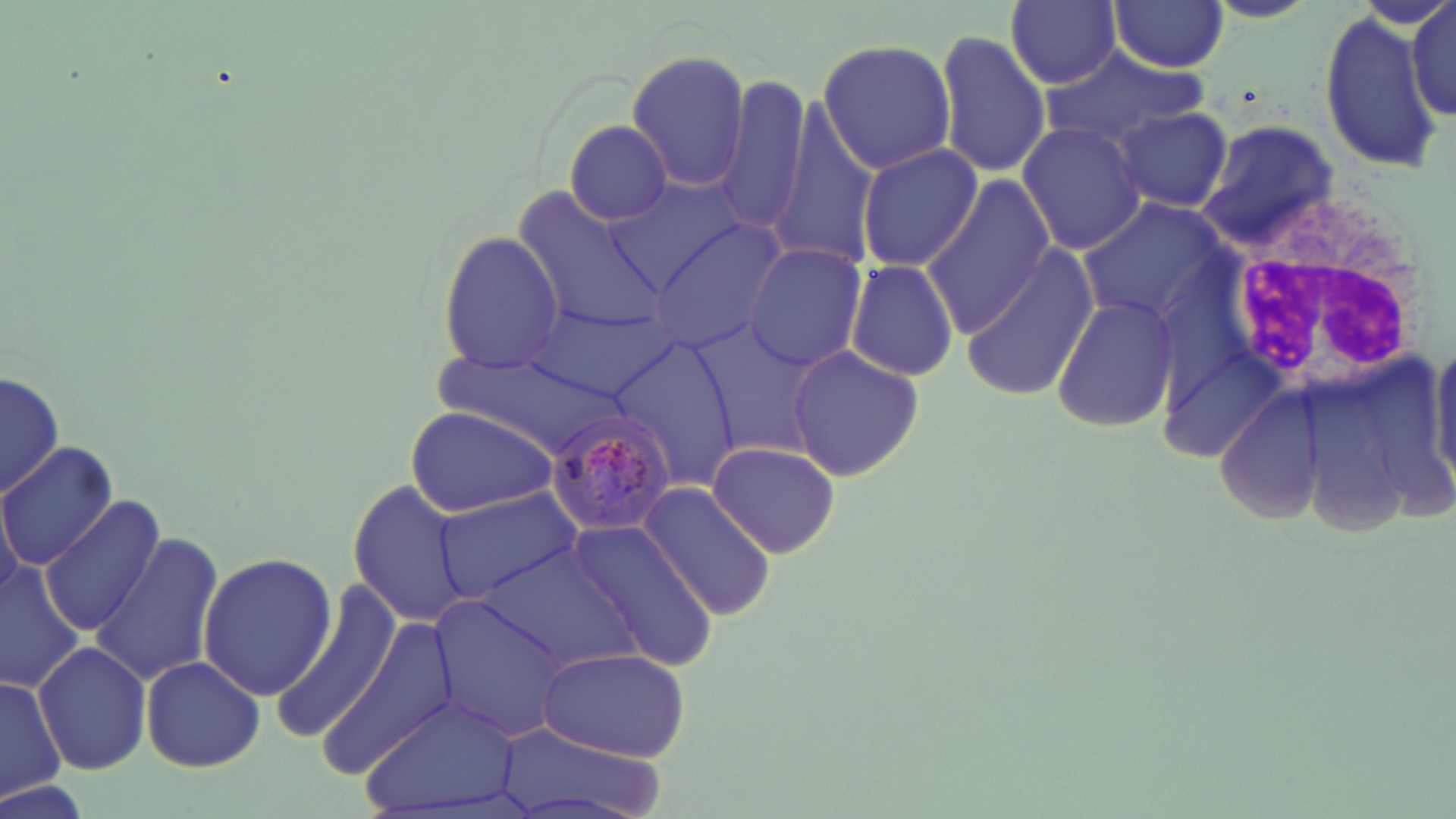

Plasmodium malariae-infected red blood cell locations = approximate bounding boxes as (x1, y1, x2, y2) in pixels: (542, 408, 677, 534)
slide-level diagnosis = Plasmodium malariae
white blood cell locations = approximate bounding boxes as (x1, y1, x2, y2) in pixels: (1206, 180, 1434, 408)
magnification = 1000x
preparation = thin blood smear
modality = light microscopy
stain = May-Grünwald-Giemsa
field of view = one of a larger specimen
image size = 1456×819 pixels
uninfected red blood cell locations = approximate bounding boxes as (x1, y1, x2, y2) in pixels: (1004, 0, 1122, 88), (1108, 0, 1229, 73), (1410, 0, 1453, 123), (1316, 6, 1443, 173), (934, 28, 1051, 179), (815, 38, 958, 176), (1037, 47, 1204, 150), (625, 50, 751, 193), (716, 75, 812, 236), (1112, 106, 1234, 213), (567, 121, 674, 226), (1016, 121, 1147, 254), (1196, 121, 1340, 247), (855, 144, 984, 274), (923, 175, 1055, 331), (611, 180, 751, 292), (513, 192, 668, 340), (1082, 200, 1228, 321), (651, 221, 791, 351), (437, 231, 565, 375), (744, 244, 869, 371), (959, 244, 1097, 402), (845, 258, 959, 382), (1051, 294, 1181, 433), (533, 300, 677, 401), (688, 319, 818, 460), (606, 336, 742, 492), (1431, 342, 1456, 485), (787, 345, 923, 482), (1, 370, 62, 503), (1209, 382, 1331, 526), (407, 405, 558, 517), (706, 440, 843, 558), (1, 441, 121, 570), (348, 481, 469, 632), (637, 482, 778, 621), (430, 485, 584, 604), (39, 497, 164, 637), (572, 522, 721, 674), (88, 533, 223, 686), (480, 544, 638, 672), (198, 552, 337, 698), (1, 563, 84, 695), (271, 588, 400, 743), (431, 596, 570, 742), (325, 616, 459, 769), (34, 641, 154, 776), (534, 648, 691, 760), (142, 654, 264, 772), (0, 676, 63, 803), (360, 693, 527, 819), (490, 722, 673, 819)